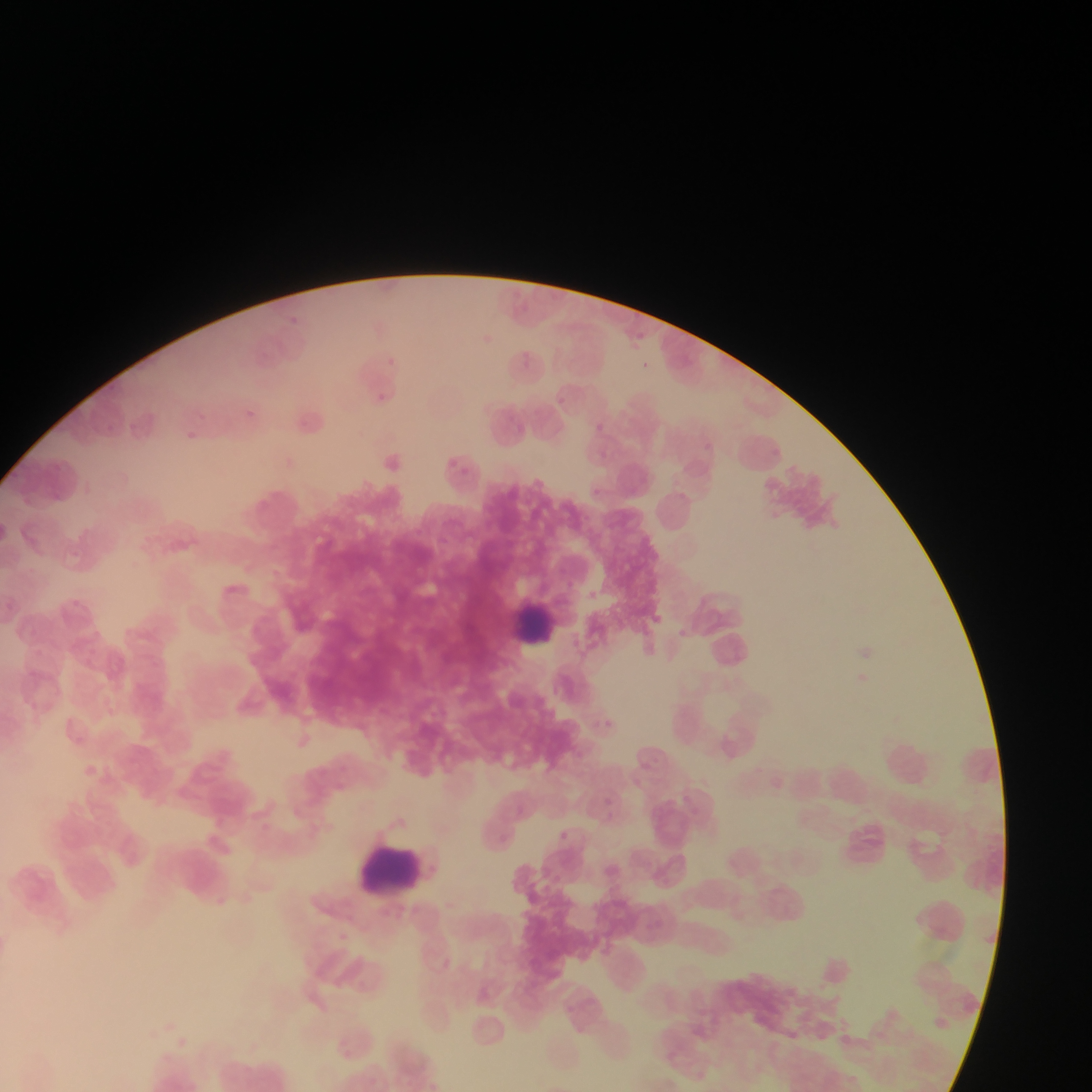 Approximate bounding boxes as {left, top, right, bottom} in pixels. Leukocyte locations: {509, 596, 571, 654}, {359, 844, 423, 901}. Plasmodium parasite locations: {286, 311, 304, 323}, {630, 327, 649, 343}, {518, 351, 540, 371}, {386, 357, 416, 375}, {641, 359, 651, 372}, {375, 390, 390, 404}, {556, 393, 568, 405}, {248, 403, 263, 423}, {200, 414, 214, 425}, {593, 419, 613, 440}, {188, 425, 199, 437}, {704, 442, 711, 450}, {600, 443, 610, 463}, {442, 457, 475, 477}, {592, 483, 603, 495}, {673, 626, 690, 648}, {855, 672, 874, 695}, {589, 713, 605, 733}, {602, 717, 621, 728}, {335, 762, 366, 784}, {628, 777, 647, 797}, {602, 791, 614, 810}, {511, 800, 528, 819}, {500, 824, 522, 849}, {559, 825, 579, 853}. Mobile-phone photograph taken through the microscope. Sample from Ghana. Image is 1092×1092 pixels. Single field of view. Thin blood film.